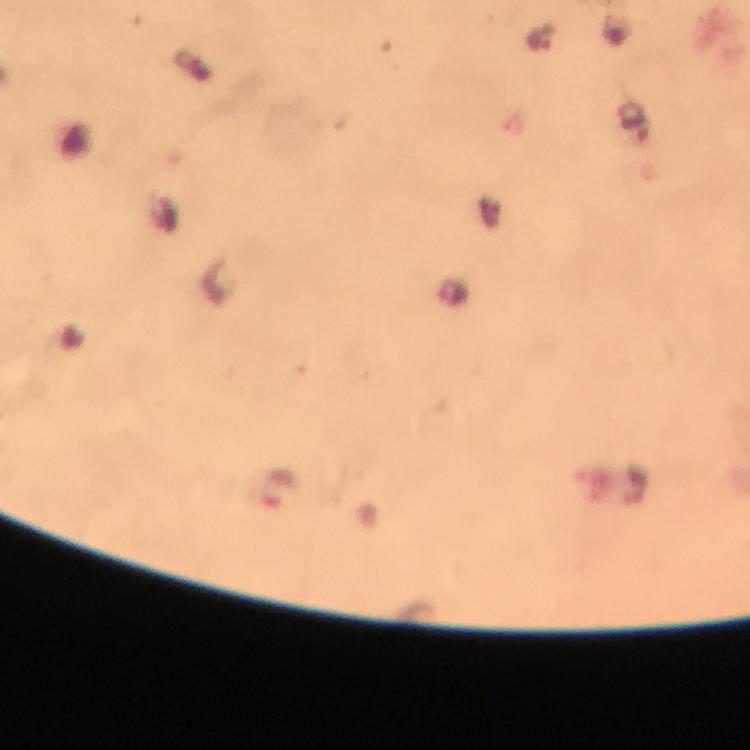
context = from a malaria diagnostic workup
stain = Giemsa
magnification = 100x
cropped from = one field of view
immersion oil = applied
malaria parasite locations = approximate centers as (x, y) in pixels: (541, 37), (454, 292), (276, 488)
image size = 750×750 pixels
capture = smartphone mounted on the microscope
preparation = thick blood smear